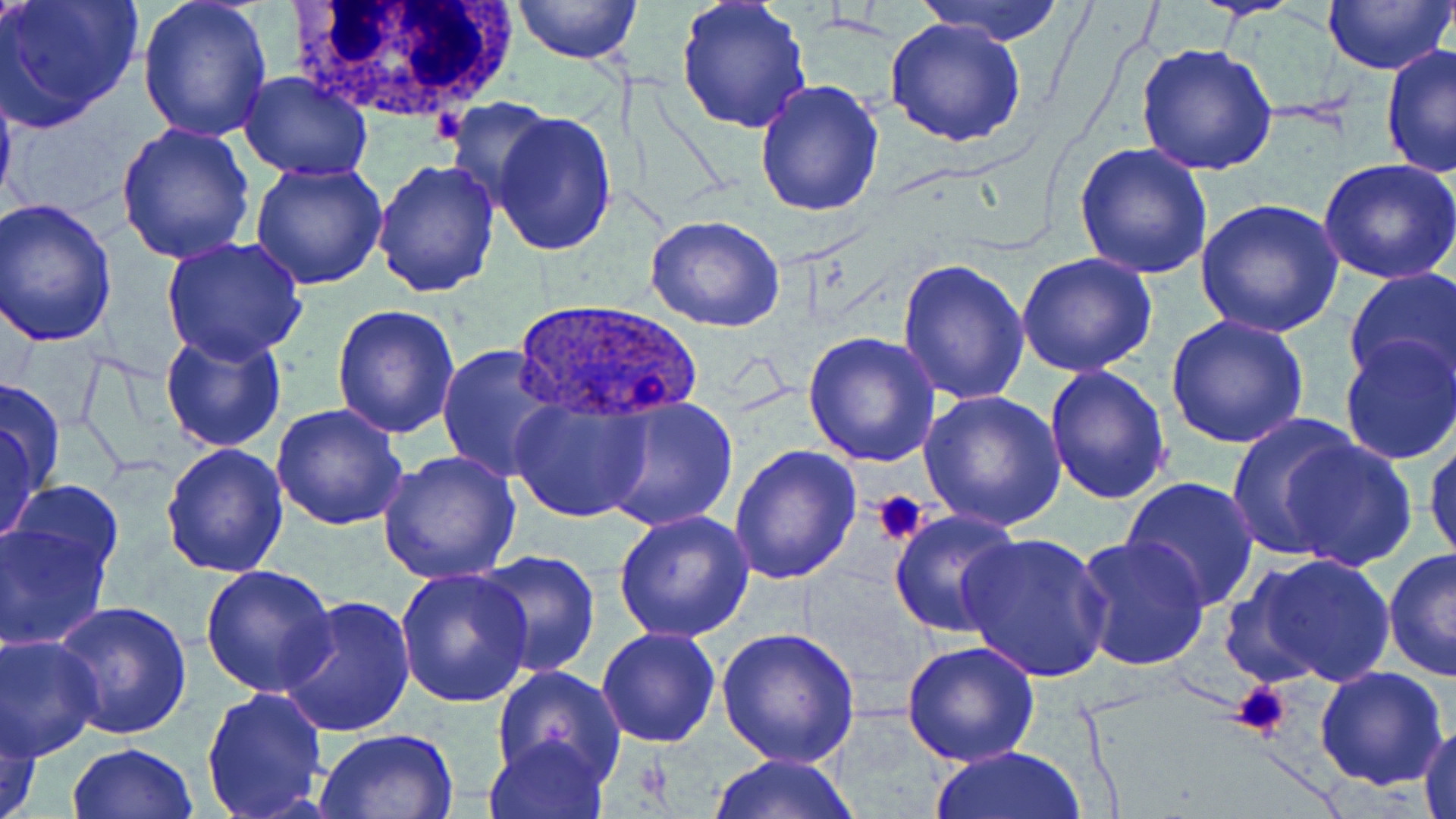

{
  "slide_level_diagnosis": "Plasmodium ovale",
  "platelet_locations": "approximate bounding boxes as named x1/y1/x2/y2 corners in pixels: (x1=872, y1=491, x2=927, y2=545), (x1=1228, y1=680, x2=1292, y2=740)",
  "stain": "May-Grünwald-Giemsa",
  "image_size": "1456×819 pixels",
  "modality": "light microscopy",
  "uninfected_red_blood_cell_locations": "approximate bounding boxes as named x1/y1/x2/y2 corners in pixels: (x1=1, y1=0, x2=145, y2=131), (x1=139, y1=0, x2=273, y2=142), (x1=512, y1=0, x2=641, y2=66), (x1=675, y1=0, x2=810, y2=136), (x1=914, y1=0, x2=1071, y2=44), (x1=1321, y1=0, x2=1455, y2=75), (x1=884, y1=17, x2=1028, y2=148), (x1=1134, y1=42, x2=1280, y2=178), (x1=1379, y1=42, x2=1456, y2=181), (x1=0, y1=59, x2=19, y2=223), (x1=239, y1=71, x2=372, y2=182), (x1=755, y1=77, x2=886, y2=216), (x1=445, y1=98, x2=557, y2=208), (x1=491, y1=111, x2=618, y2=257), (x1=114, y1=124, x2=257, y2=267), (x1=1074, y1=142, x2=1213, y2=280), (x1=373, y1=159, x2=500, y2=297), (x1=1318, y1=159, x2=1456, y2=284), (x1=247, y1=160, x2=389, y2=289), (x1=2, y1=199, x2=119, y2=345), (x1=1196, y1=199, x2=1344, y2=339), (x1=644, y1=216, x2=788, y2=332), (x1=161, y1=236, x2=308, y2=363), (x1=1016, y1=253, x2=1158, y2=377), (x1=897, y1=257, x2=1030, y2=404), (x1=1345, y1=266, x2=1456, y2=391), (x1=330, y1=303, x2=460, y2=438), (x1=1166, y1=313, x2=1312, y2=449), (x1=160, y1=328, x2=289, y2=455), (x1=803, y1=332, x2=941, y2=468), (x1=1337, y1=334, x2=1455, y2=466), (x1=438, y1=344, x2=567, y2=482), (x1=1043, y1=365, x2=1171, y2=505), (x1=1, y1=375, x2=67, y2=505), (x1=919, y1=388, x2=1067, y2=531), (x1=509, y1=395, x2=654, y2=525), (x1=594, y1=395, x2=740, y2=533), (x1=271, y1=405, x2=409, y2=532), (x1=0, y1=406, x2=46, y2=552), (x1=1226, y1=418, x2=1362, y2=562), (x1=1425, y1=432, x2=1456, y2=568), (x1=1279, y1=438, x2=1416, y2=570), (x1=162, y1=443, x2=291, y2=579), (x1=728, y1=444, x2=861, y2=585), (x1=376, y1=449, x2=519, y2=584), (x1=1120, y1=476, x2=1263, y2=613), (x1=7, y1=482, x2=124, y2=578), (x1=888, y1=509, x2=1025, y2=641), (x1=612, y1=511, x2=755, y2=645), (x1=0, y1=521, x2=111, y2=651), (x1=958, y1=531, x2=1113, y2=683), (x1=1073, y1=533, x2=1211, y2=670), (x1=473, y1=550, x2=601, y2=678), (x1=1382, y1=550, x2=1456, y2=681), (x1=1244, y1=552, x2=1398, y2=689), (x1=201, y1=565, x2=337, y2=698), (x1=396, y1=568, x2=533, y2=708), (x1=279, y1=595, x2=415, y2=738), (x1=52, y1=601, x2=194, y2=741), (x1=715, y1=625, x2=862, y2=766), (x1=596, y1=626, x2=722, y2=748), (x1=1, y1=635, x2=103, y2=761), (x1=900, y1=641, x2=1042, y2=768), (x1=491, y1=666, x2=624, y2=787), (x1=1314, y1=666, x2=1449, y2=790), (x1=201, y1=684, x2=328, y2=818), (x1=1, y1=700, x2=43, y2=819), (x1=1415, y1=721, x2=1456, y2=818), (x1=314, y1=728, x2=457, y2=817), (x1=484, y1=731, x2=609, y2=819), (x1=65, y1=742, x2=199, y2=819), (x1=929, y1=744, x2=1088, y2=818), (x1=706, y1=751, x2=863, y2=819)",
  "magnification": "1000x",
  "white_blood_cell_locations": "approximate bounding boxes as named x1/y1/x2/y2 corners in pixels: (x1=292, y1=0, x2=518, y2=132)",
  "preparation": "thin blood smear",
  "field_of_view": "one of a larger specimen",
  "plasmodium_ovale_infected_red_blood_cell_locations": "approximate bounding boxes as named x1/y1/x2/y2 corners in pixels: (x1=515, y1=299, x2=700, y2=427)"
}